Assess the morphology of the erythrocytes.
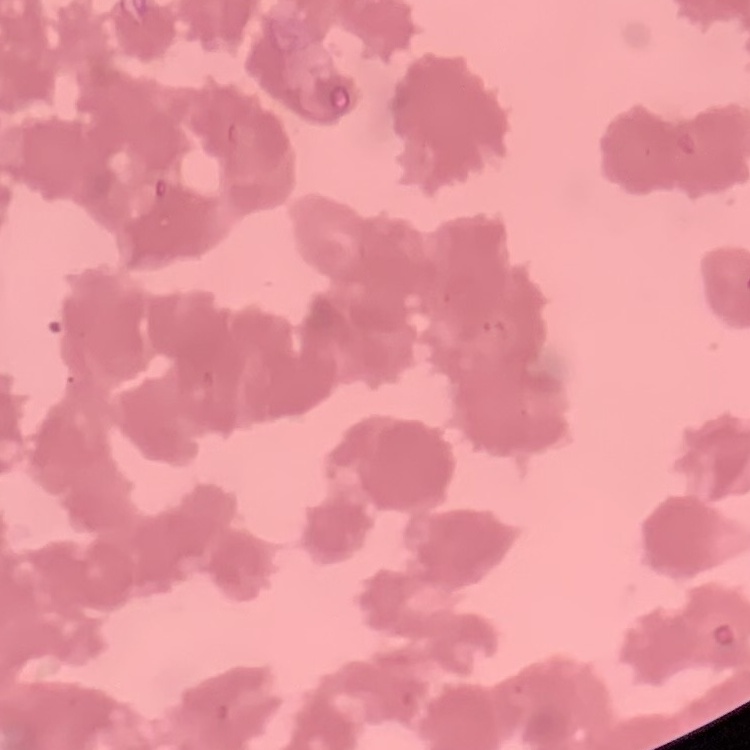
They show rouleaux formation.

Square crop of a larger photomicrograph. Thin blood film. Field's or Giemsa stain.